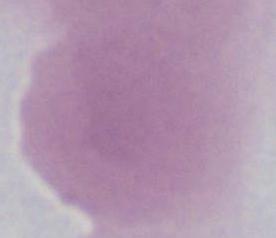

Captured at 1000x magnification. A red blood cell is seen. Photomicrograph.